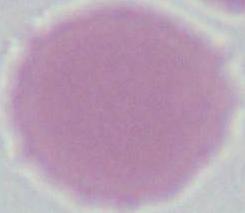
Summary:
  - Magnification: 1000x
  - Identification: erythrocyte
  - Modality: photomicrograph